Locate and identify every blood parasite.
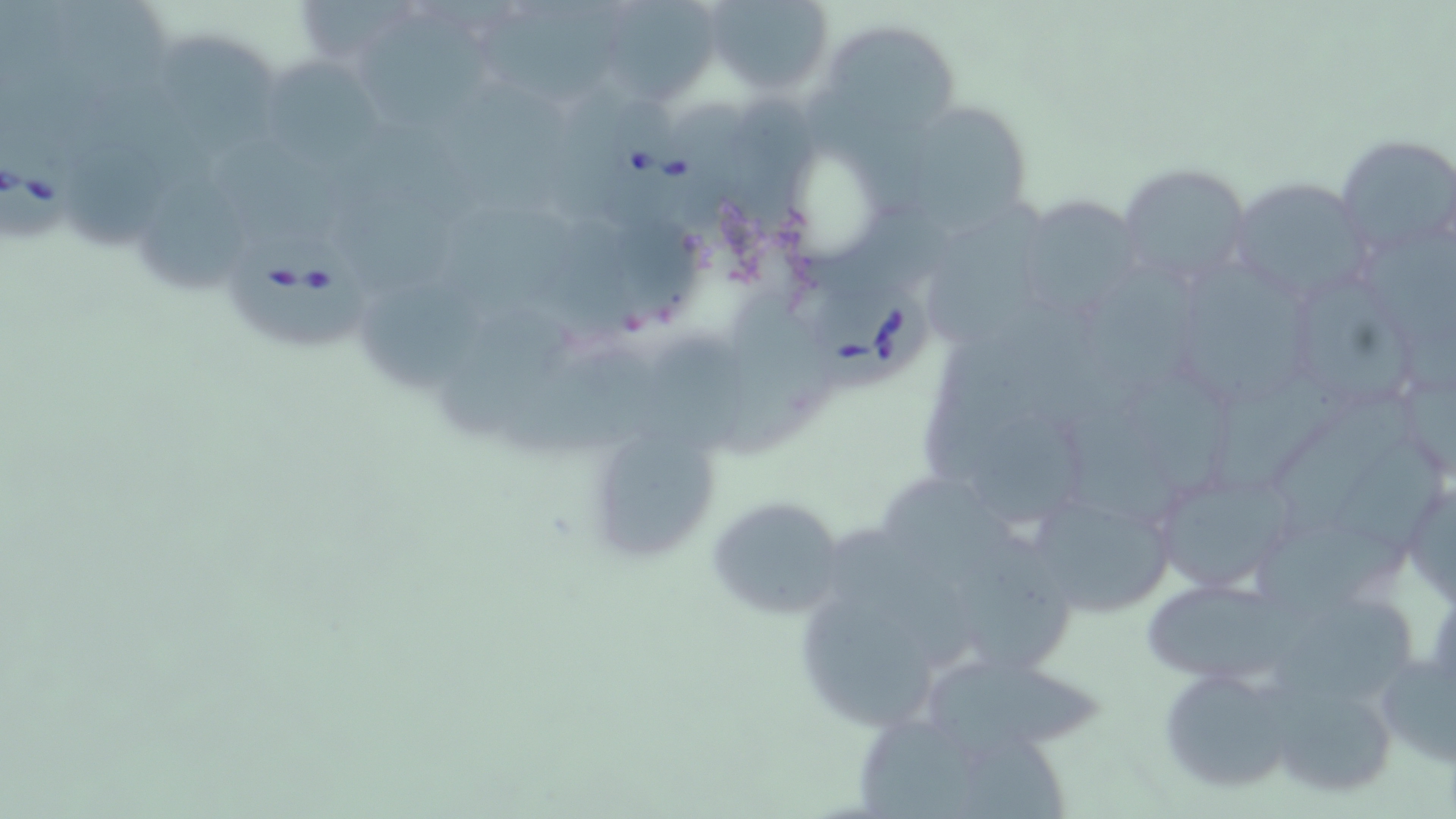
Approximate bounding boxes as [x1, y1, x2, y2] in pixels.
Babesia divergens-infected red blood cells: [602, 98, 694, 230], [0, 128, 80, 241], [228, 229, 378, 352], [814, 290, 934, 395].
No Plasmodium falciparum, Plasmodium ovale, Plasmodium malariae, Plasmodium vivax, or Trypanosoma brucei observed.

Summary:
  - Uninfected red blood cell locations: [705, 0, 832, 92], [484, 10, 625, 96], [610, 10, 717, 102], [358, 15, 505, 133], [817, 18, 961, 138], [161, 41, 302, 154], [265, 64, 395, 161], [456, 81, 584, 220], [897, 98, 1033, 229], [735, 100, 831, 226], [1334, 133, 1456, 262], [58, 141, 175, 249], [1119, 162, 1254, 288], [1227, 178, 1369, 301], [141, 181, 250, 296], [1017, 197, 1145, 319], [929, 206, 1049, 344], [1189, 260, 1312, 412], [1091, 262, 1222, 402], [1300, 279, 1418, 407], [368, 280, 486, 390], [717, 285, 837, 460], [443, 305, 580, 439], [639, 336, 757, 458], [501, 346, 658, 466], [1207, 373, 1345, 499], [1281, 386, 1420, 535], [971, 418, 1094, 527], [604, 431, 722, 563], [1318, 438, 1448, 548], [1150, 467, 1297, 594], [1403, 469, 1456, 611], [883, 474, 1020, 573], [1027, 486, 1178, 617], [707, 494, 846, 622], [1243, 519, 1416, 618], [828, 529, 980, 672], [953, 535, 1089, 682], [1147, 579, 1305, 675], [1278, 595, 1417, 702], [797, 599, 932, 729], [1377, 638, 1456, 773], [927, 662, 1107, 751], [1156, 664, 1297, 794], [1265, 678, 1403, 801]
  - Slide-level diagnosis: Babesia divergens
  - Modality: optical microscopy
  - Magnification: 1000x
  - Stain: May-Grünwald-Giemsa
  - Image size: 1456×819 pixels
  - Preparation: thin blood film
  - Field of view: one of a larger specimen